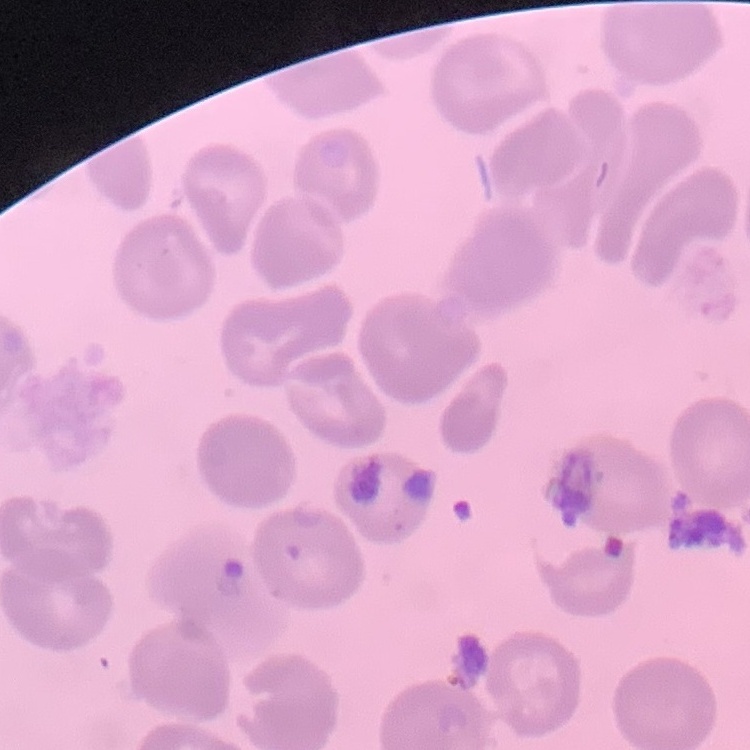
Summary:
  - Erythrocyte morphology: no rouleaux formation
  - Stain: Field's or Giemsa
  - Image type: square crop of a larger photomicrograph
  - Preparation: thin blood film